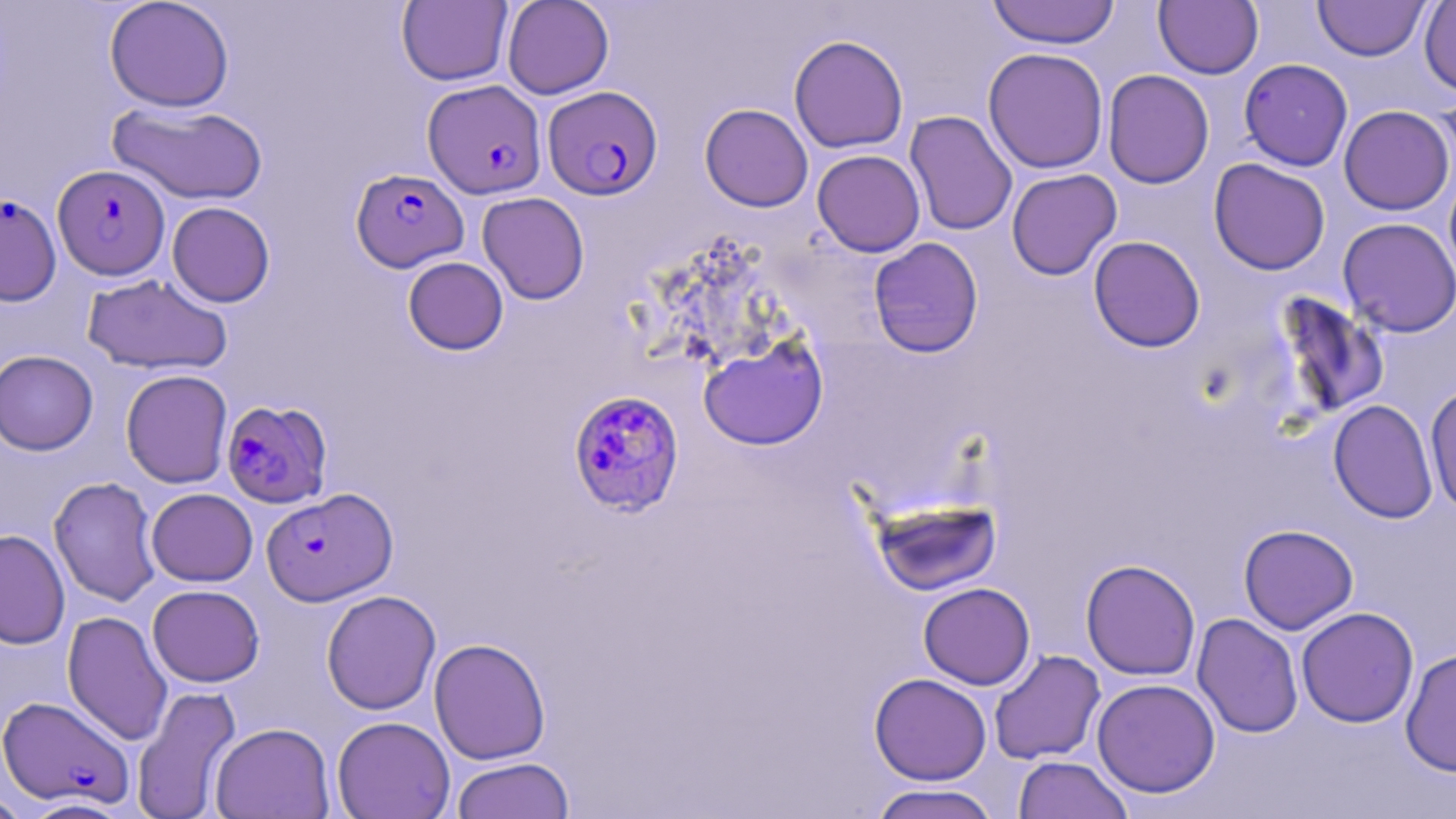

Summary:
  - Coordinate format: approximate bounding boxes as [x1, y1, x2, y2] in pixels
  - Uninfected red blood cell locations: [104, 0, 234, 112], [502, 0, 614, 99], [987, 0, 1121, 49], [1154, 0, 1263, 79], [1313, 0, 1430, 61], [1419, 0, 1456, 96], [397, 1, 512, 86], [788, 34, 909, 153], [983, 47, 1109, 174], [1238, 58, 1353, 171], [1102, 69, 1214, 189], [1434, 89, 1456, 190], [107, 101, 268, 205], [700, 103, 813, 212], [1339, 105, 1454, 215], [904, 110, 1018, 236], [812, 149, 925, 257], [1208, 158, 1331, 275], [1006, 168, 1122, 281], [1443, 169, 1456, 290], [477, 192, 590, 304], [166, 201, 275, 307], [1337, 217, 1456, 338], [1088, 236, 1205, 353], [868, 237, 984, 357], [403, 256, 508, 355], [82, 272, 233, 376], [1271, 291, 1391, 422], [699, 335, 828, 450], [0, 350, 98, 455], [120, 369, 233, 488], [1424, 385, 1456, 516], [1328, 399, 1438, 523], [48, 476, 161, 607], [147, 488, 257, 586], [871, 496, 1002, 595], [1238, 524, 1358, 634], [0, 530, 70, 649], [1080, 559, 1201, 680], [918, 582, 1035, 690], [147, 584, 265, 687], [321, 590, 440, 715], [1296, 606, 1419, 727], [62, 610, 173, 746], [1191, 613, 1303, 738], [429, 637, 550, 764], [1400, 648, 1456, 777], [989, 649, 1105, 765], [869, 673, 992, 785], [1091, 678, 1220, 797], [131, 685, 241, 818], [332, 715, 455, 819], [210, 722, 334, 818], [1013, 756, 1133, 819], [450, 757, 575, 819], [868, 783, 1001, 819], [0, 791, 32, 819], [20, 797, 133, 818]
  - Plasmodium falciparum-infected red blood cell locations: [422, 79, 547, 199], [543, 85, 662, 201], [53, 164, 170, 280], [351, 169, 469, 272], [0, 193, 62, 307], [568, 389, 685, 517], [221, 398, 332, 508], [261, 487, 397, 605], [0, 695, 135, 808]
  - Slide-level diagnosis: Plasmodium falciparum
  - Preparation: thin blood smear
  - Modality: optical microscopy
  - Stain: May-Grünwald-Giemsa
  - Field of view: one of a larger specimen
  - Image size: 1456×819 pixels
  - Magnification: 1000x